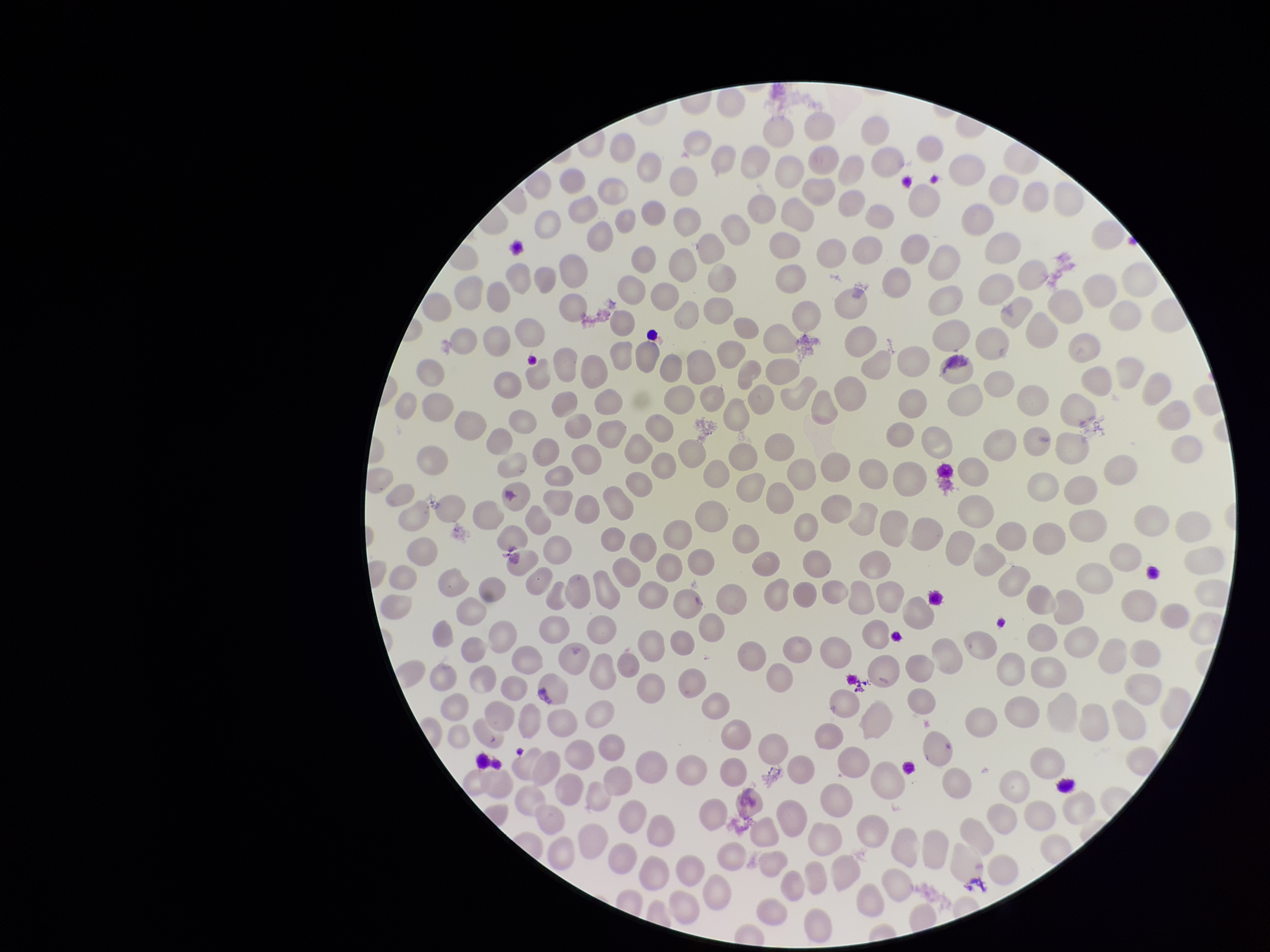
parasitized red blood cell count = 0
image size = 1270×952 pixels
field of view = one from this slide
preparation = thin smear
capture = smartphone photograph through the microscope eyepiece
patient malaria status = negative
red blood cell count = 267
stain = Giemsa
parasitized red blood cells = none detected